Name the parasite shown.
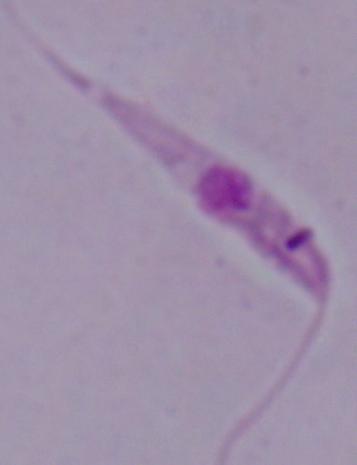
This is Leishmania.

modality = micrograph
magnification = 1000x